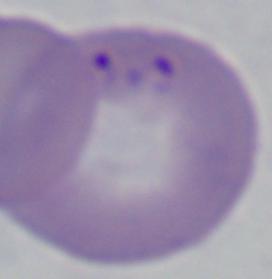
Summary:
  - Identification: Babesia
  - Magnification: 1000x
  - Modality: micrograph